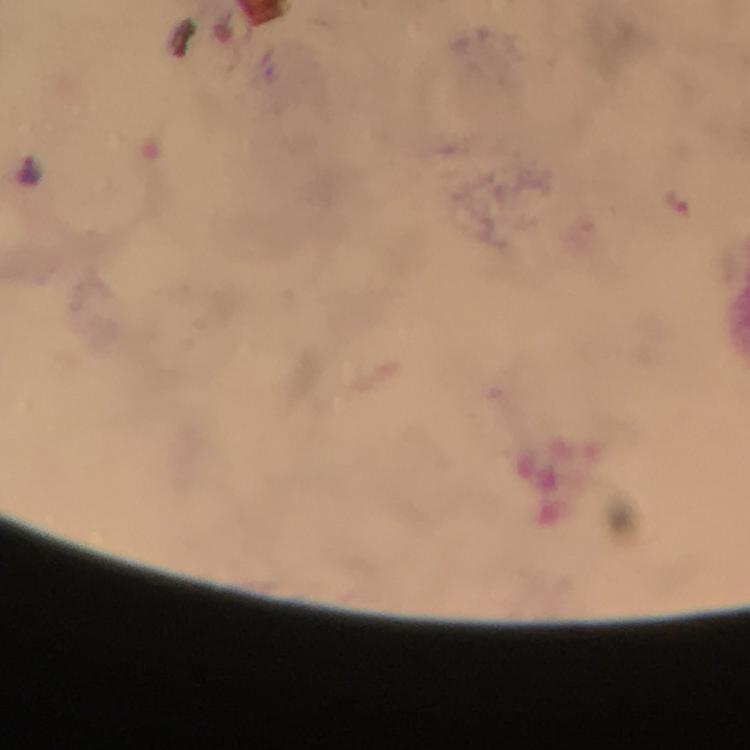

Approximate centers as [x, y] in pixels. Malaria parasite locations: [30, 169]. Image is 750×750 pixels. From a diagnostic examination for malaria. Immersion oil applied. Cropped region of a single field of view. At 100x magnification. Thick blood smear. Smartphone photograph taken through a microscope. Giemsa-stained preparation.